Identify the preparation type.
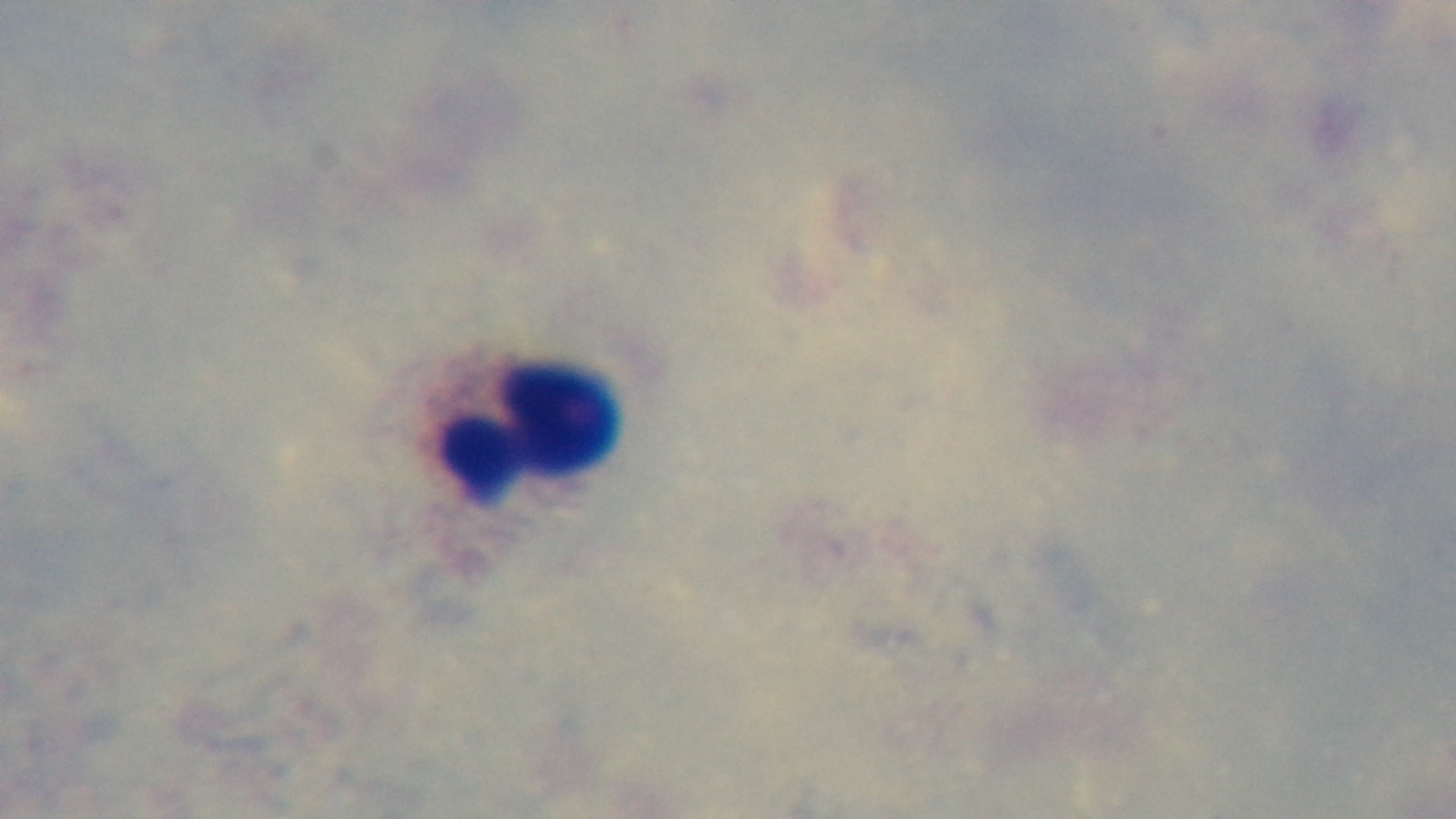
A thick smear.

stain = Giemsa
modality = light microscopy
capture = mounted 4K digital camera
malaria status = uninfected
field of view = one from the slide
objective = 100x oil immersion